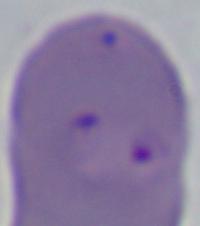 Micrograph. A Babesia parasite is seen. 1000x magnification.